Report the malaria status of this cell.
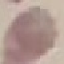
It is uninfected.

Giemsa stain. Automatically extracted cell patch, resized to 64 × 64 pixels. Photographed with a smartphone camera at the microscope eyepiece. Thin smear of blood.